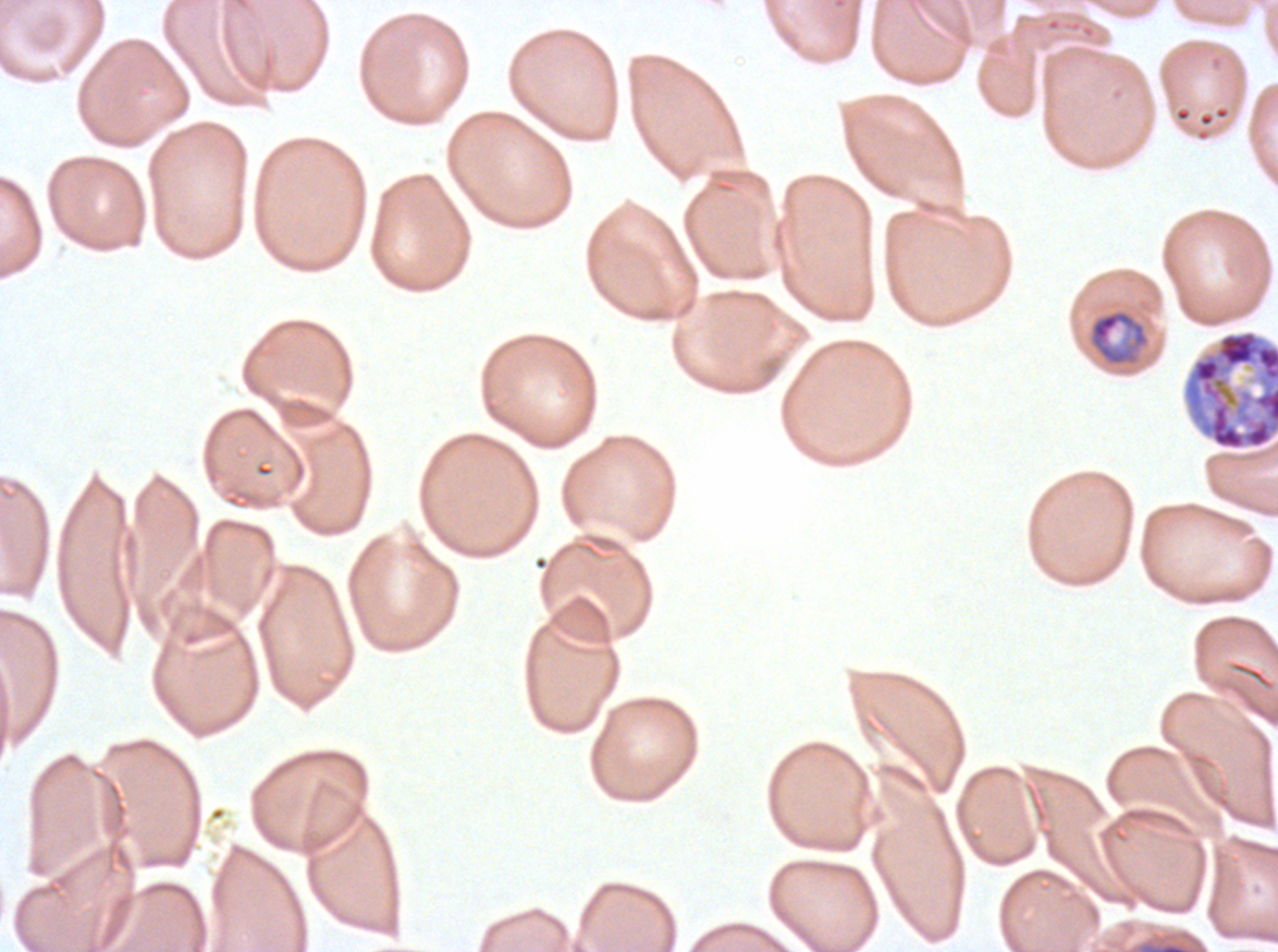
Approximate bounding boxes as {x1, y1, x2, y2} in pixels. Late schizont locations: {1182, 329, 1277, 451}. Mid trophozoite locations: {1088, 309, 1149, 367}. Thin blood film. Image is 1278×952 pixels. Life-cycle stages observed: mid trophozoite, late schizont. Giemsa-stained preparation. One sub-image of a larger composite. Ex-vivo P. falciparum culture from a patient in The Gambia, grown for 24 to 48 hours.